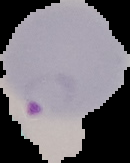
Summary:
  - Preparation: thin blood smear
  - Image type: segmented cell region on a black background
  - Result: malaria parasites identified
  - Image size: 130×163 pixels